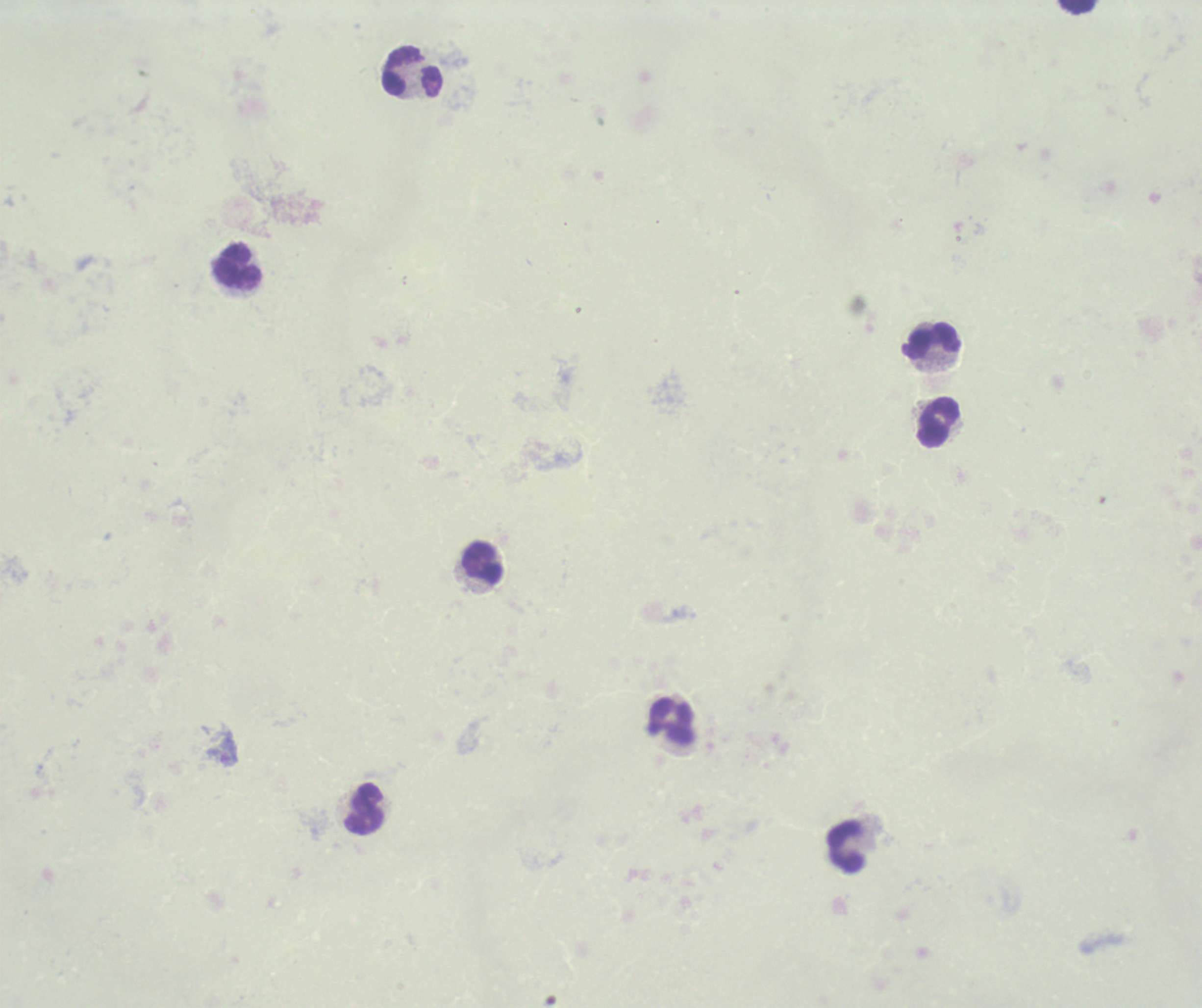

Approximate centers as (x, y) in pixels.
Summary:
  - Leukocyte locations: (1078, 7), (412, 72), (236, 266), (930, 342), (939, 423), (483, 564), (671, 721), (365, 807), (845, 847)
  - Image size: 1202×1008 pixels
  - Context: previously used in a real diagnosis
  - Preparation: thick smear of blood
  - Field of view: single
  - Stain: Romanowsky
  - Magnification: 100x
  - Background quality: unsatisfactory
  - Result: no Plasmodium parasites detected